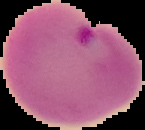
image_type: cell region segmented out of the field of view; surrounding area masked to black
preparation: thin blood film
image_size: 145×130 pixels
result: Plasmodium parasites identified